Name the blood parasite species.
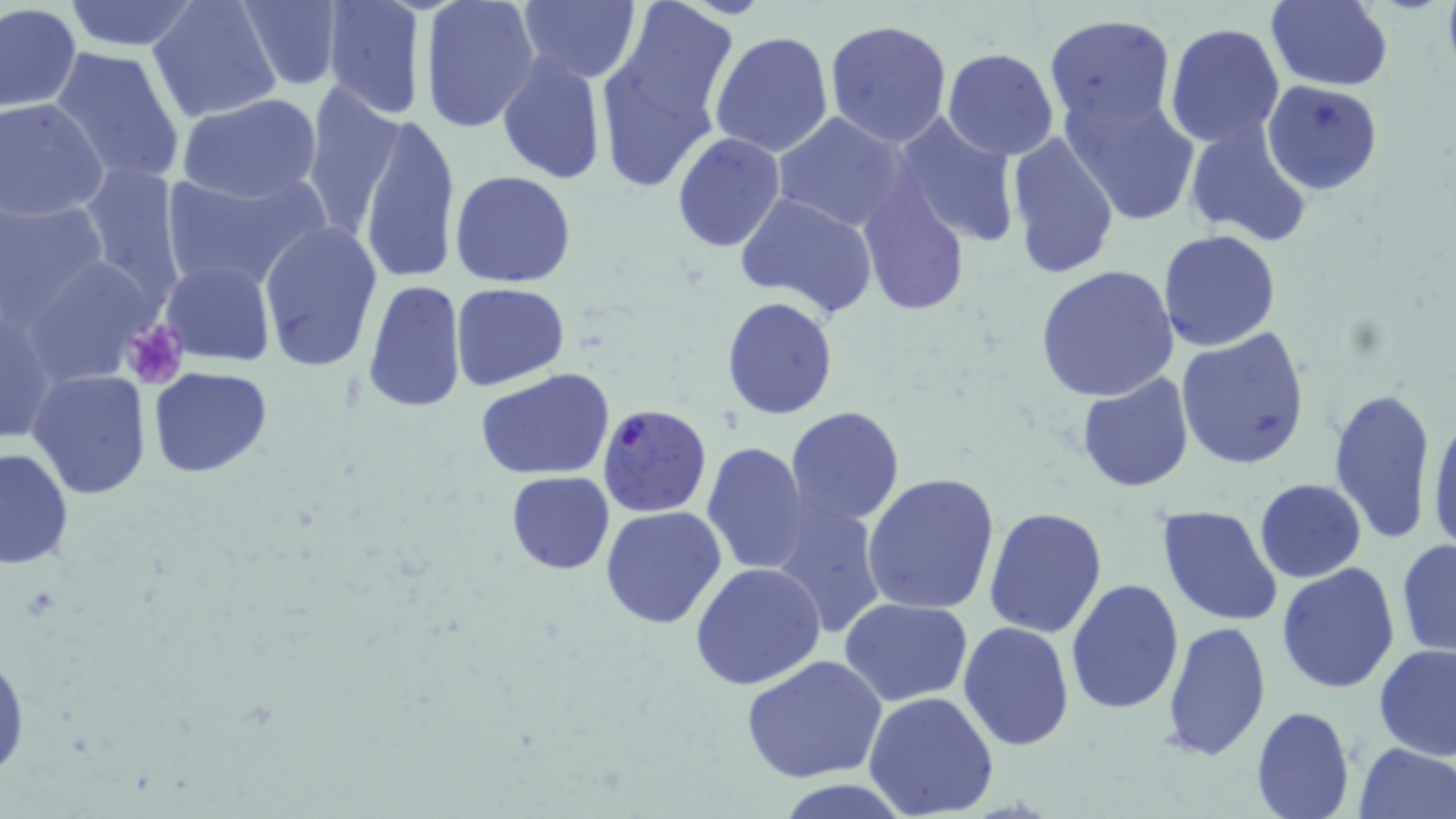

Plasmodium falciparum.

Summary:
  - Coordinate format: approximate bounding boxes as [x1, y1, x2, y2] in pixels
  - Platelet locations: [120, 318, 187, 390]
  - Uninfected red blood cell locations: [61, 0, 202, 52], [148, 0, 282, 123], [234, 0, 344, 90], [515, 0, 640, 84], [1263, 0, 1393, 91], [321, 1, 426, 121], [421, 1, 542, 134], [611, 2, 737, 126], [0, 4, 82, 112], [1044, 15, 1178, 131], [823, 18, 953, 146], [1165, 23, 1285, 148], [710, 30, 834, 156], [593, 32, 729, 195], [47, 46, 187, 187], [942, 49, 1061, 161], [497, 50, 607, 185], [1263, 80, 1383, 194], [298, 83, 404, 235], [1063, 86, 1198, 226], [176, 94, 322, 204], [1, 98, 108, 220], [772, 111, 913, 236], [891, 112, 1021, 248], [355, 116, 461, 286], [1183, 119, 1315, 247], [1003, 129, 1121, 280], [671, 133, 786, 251], [79, 161, 185, 303], [159, 167, 327, 294], [450, 170, 576, 289], [855, 183, 971, 315], [734, 192, 880, 318], [0, 194, 109, 328], [260, 222, 382, 371], [1158, 230, 1283, 352], [161, 259, 274, 366], [1036, 264, 1179, 402], [362, 279, 468, 415], [451, 282, 569, 390], [721, 296, 839, 420], [1175, 329, 1312, 470], [147, 365, 271, 477], [475, 368, 617, 480], [28, 369, 150, 501], [1075, 373, 1194, 493], [1329, 385, 1440, 543], [1427, 403, 1456, 556], [785, 406, 906, 529], [701, 440, 810, 576], [1, 447, 75, 569], [506, 471, 615, 575], [863, 471, 1003, 616], [1254, 479, 1365, 583], [772, 503, 886, 640], [1157, 504, 1284, 627], [600, 505, 727, 629], [985, 505, 1109, 638], [1396, 539, 1456, 658], [690, 561, 826, 690], [1277, 562, 1401, 694], [1065, 577, 1183, 714], [839, 597, 972, 706], [1160, 619, 1271, 763], [957, 621, 1074, 752], [0, 638, 28, 781], [1375, 645, 1456, 762], [741, 654, 887, 783], [864, 690, 1000, 818], [1249, 704, 1356, 819], [1354, 740, 1456, 819], [778, 779, 911, 818]
  - Plasmodium falciparum-infected red blood cell locations: [597, 404, 711, 519]
  - Stain: May-Grünwald-Giemsa
  - Modality: optical microscopy
  - Preparation: thin blood film
  - Image size: 1456×819 pixels
  - Field of view: one of a larger specimen
  - Magnification: 1000x